Point out each Plasmodium parasite.
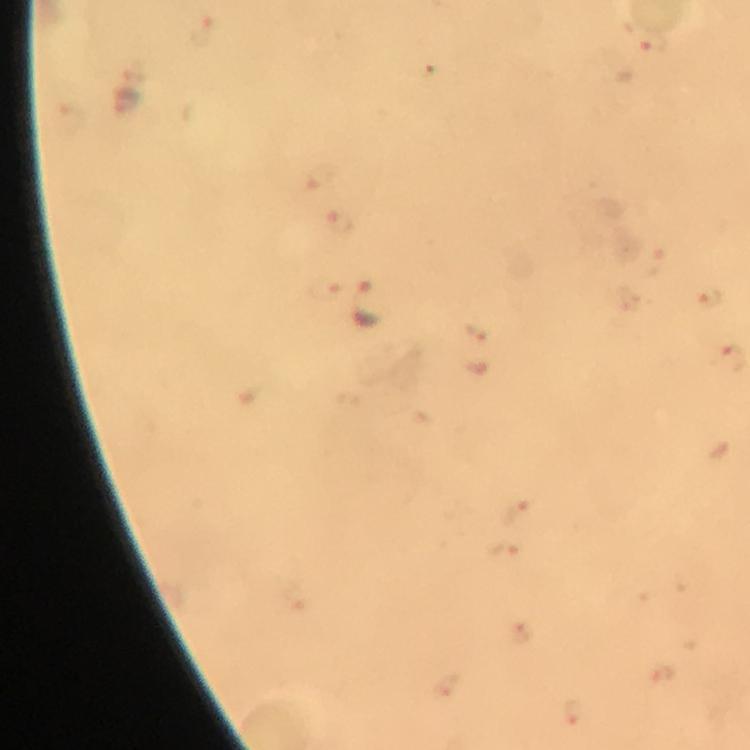
Approximate centers as [x, y] in pixels.
Plasmodium parasites: [201, 33], [652, 41], [127, 104], [321, 179], [341, 222], [652, 260], [326, 289], [708, 299], [368, 306], [475, 335], [730, 359], [516, 510], [505, 550], [522, 635], [448, 688], [573, 711].

Summary:
  - Cropped from: one field of view
  - Context: from a diagnostic examination for malaria
  - Immersion oil: used
  - Capture: smartphone camera through the microscope
  - Magnification: 100x
  - Image size: 750×750 pixels
  - Preparation: thick blood smear
  - Stain: Giemsa